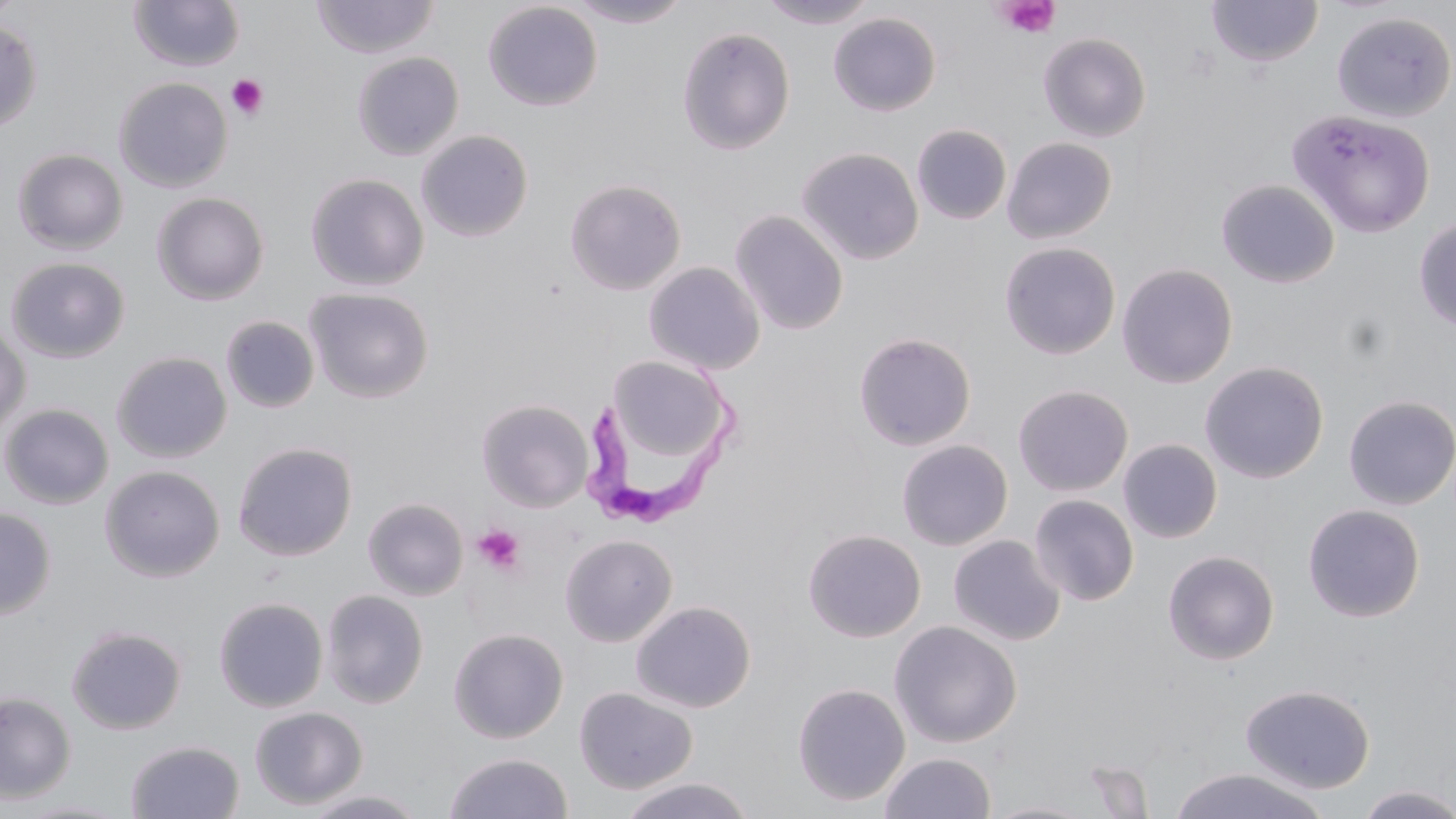

Summary:
  - Coordinate format: approximate bounding boxes as named x1/y1/x2/y2 corners in pixels
  - Platelet locations: (x1=995, y1=0, x2=1060, y2=39), (x1=226, y1=74, x2=269, y2=120), (x1=472, y1=524, x2=527, y2=575)
  - Trypanosoma brucei locations: (x1=589, y1=358, x2=747, y2=532)
  - Uninfected red blood cell locations: (x1=311, y1=0, x2=440, y2=59), (x1=565, y1=0, x2=694, y2=28), (x1=757, y1=0, x2=880, y2=29), (x1=1206, y1=0, x2=1324, y2=67), (x1=127, y1=1, x2=246, y2=71), (x1=482, y1=2, x2=604, y2=111), (x1=827, y1=12, x2=942, y2=116), (x1=1332, y1=12, x2=1455, y2=123), (x1=0, y1=18, x2=42, y2=133), (x1=676, y1=26, x2=795, y2=155), (x1=1038, y1=32, x2=1151, y2=142), (x1=351, y1=52, x2=464, y2=160), (x1=114, y1=77, x2=233, y2=192), (x1=1288, y1=109, x2=1435, y2=238), (x1=911, y1=124, x2=1012, y2=225), (x1=416, y1=130, x2=534, y2=242), (x1=1002, y1=136, x2=1117, y2=244), (x1=797, y1=147, x2=923, y2=265), (x1=12, y1=148, x2=128, y2=254), (x1=305, y1=174, x2=428, y2=290), (x1=565, y1=179, x2=686, y2=295), (x1=1216, y1=179, x2=1340, y2=288), (x1=151, y1=192, x2=269, y2=304), (x1=729, y1=209, x2=849, y2=335), (x1=1414, y1=215, x2=1456, y2=333), (x1=999, y1=242, x2=1121, y2=359), (x1=5, y1=257, x2=131, y2=363), (x1=644, y1=262, x2=765, y2=375), (x1=1117, y1=263, x2=1238, y2=388), (x1=304, y1=287, x2=434, y2=403), (x1=220, y1=316, x2=320, y2=413), (x1=0, y1=323, x2=31, y2=439), (x1=853, y1=332, x2=976, y2=450), (x1=111, y1=351, x2=231, y2=463), (x1=608, y1=356, x2=730, y2=462), (x1=1199, y1=361, x2=1329, y2=483), (x1=1012, y1=384, x2=1133, y2=496), (x1=1342, y1=395, x2=1456, y2=510), (x1=476, y1=399, x2=594, y2=512), (x1=1, y1=403, x2=114, y2=510), (x1=896, y1=439, x2=1013, y2=550), (x1=1119, y1=439, x2=1223, y2=544), (x1=232, y1=441, x2=357, y2=561), (x1=100, y1=465, x2=225, y2=582), (x1=1029, y1=494, x2=1139, y2=606), (x1=363, y1=497, x2=469, y2=601), (x1=1302, y1=503, x2=1425, y2=622), (x1=0, y1=507, x2=56, y2=621), (x1=802, y1=529, x2=927, y2=643), (x1=559, y1=534, x2=678, y2=647), (x1=948, y1=535, x2=1065, y2=645), (x1=1162, y1=550, x2=1280, y2=665), (x1=320, y1=589, x2=429, y2=708), (x1=213, y1=596, x2=329, y2=712), (x1=630, y1=600, x2=756, y2=713), (x1=889, y1=620, x2=1022, y2=748), (x1=65, y1=625, x2=187, y2=735), (x1=448, y1=628, x2=568, y2=743), (x1=791, y1=682, x2=911, y2=806), (x1=1240, y1=683, x2=1376, y2=794), (x1=574, y1=687, x2=698, y2=794), (x1=0, y1=692, x2=76, y2=803), (x1=249, y1=707, x2=368, y2=810), (x1=125, y1=739, x2=245, y2=819), (x1=444, y1=752, x2=573, y2=818), (x1=879, y1=752, x2=995, y2=819), (x1=1167, y1=767, x2=1330, y2=819), (x1=618, y1=776, x2=755, y2=818), (x1=1355, y1=785, x2=1456, y2=819), (x1=301, y1=789, x2=428, y2=818), (x1=10, y1=799, x2=132, y2=818), (x1=984, y1=800, x2=1098, y2=818)
  - Slide-level diagnosis: Trypanosoma brucei
  - Image size: 1456×819 pixels
  - Modality: optical microscopy
  - Magnification: 1000x
  - Field of view: one of a larger specimen
  - Stain: May-Grünwald-Giemsa
  - Preparation: thin blood film